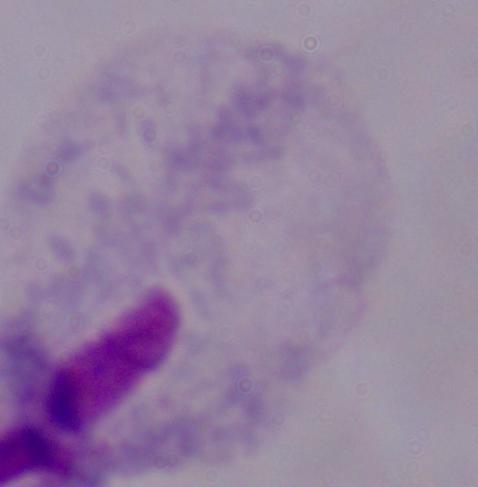

modality = micrograph
magnification = 1000x
identification = trichomonad